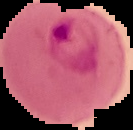
Summary:
  - Malaria status: parasitized
  - Image type: segmented cell region on a black background
  - Image size: 133×130 pixels
  - Preparation: thin blood smear